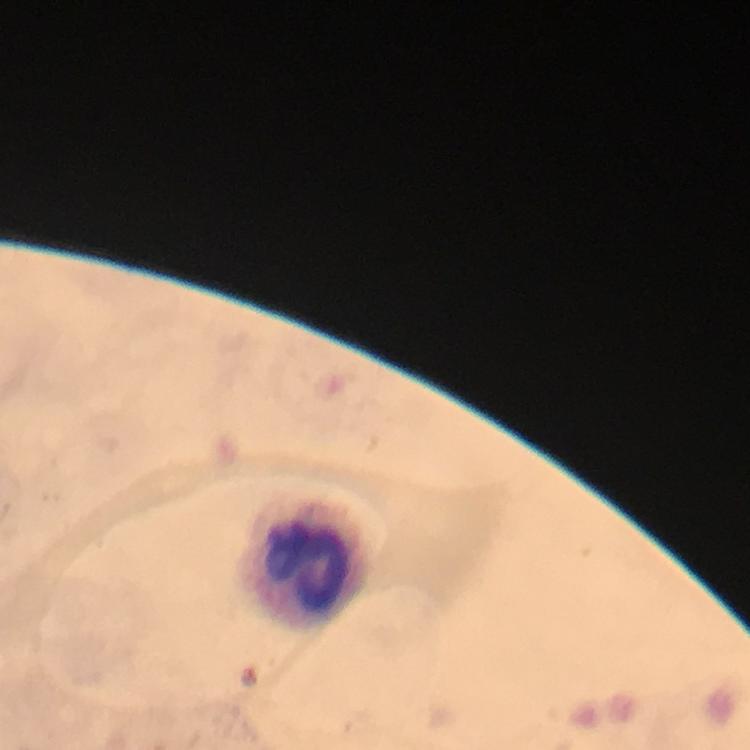

{
  "stain": "Giemsa",
  "preparation": "thick blood smear",
  "immersion_oil": "applied",
  "capture": "smartphone camera through the microscope",
  "cropped_from": "a single field of view",
  "plasmodium_parasites": "none seen",
  "leukocyte_locations": "approximate object centers, in pixels from the top-left corner: (x=306, y=567)",
  "image_size": "750×750 pixels",
  "magnification": "100x",
  "context": "from a diagnostic examination for malaria"
}